State the blood parasite species.
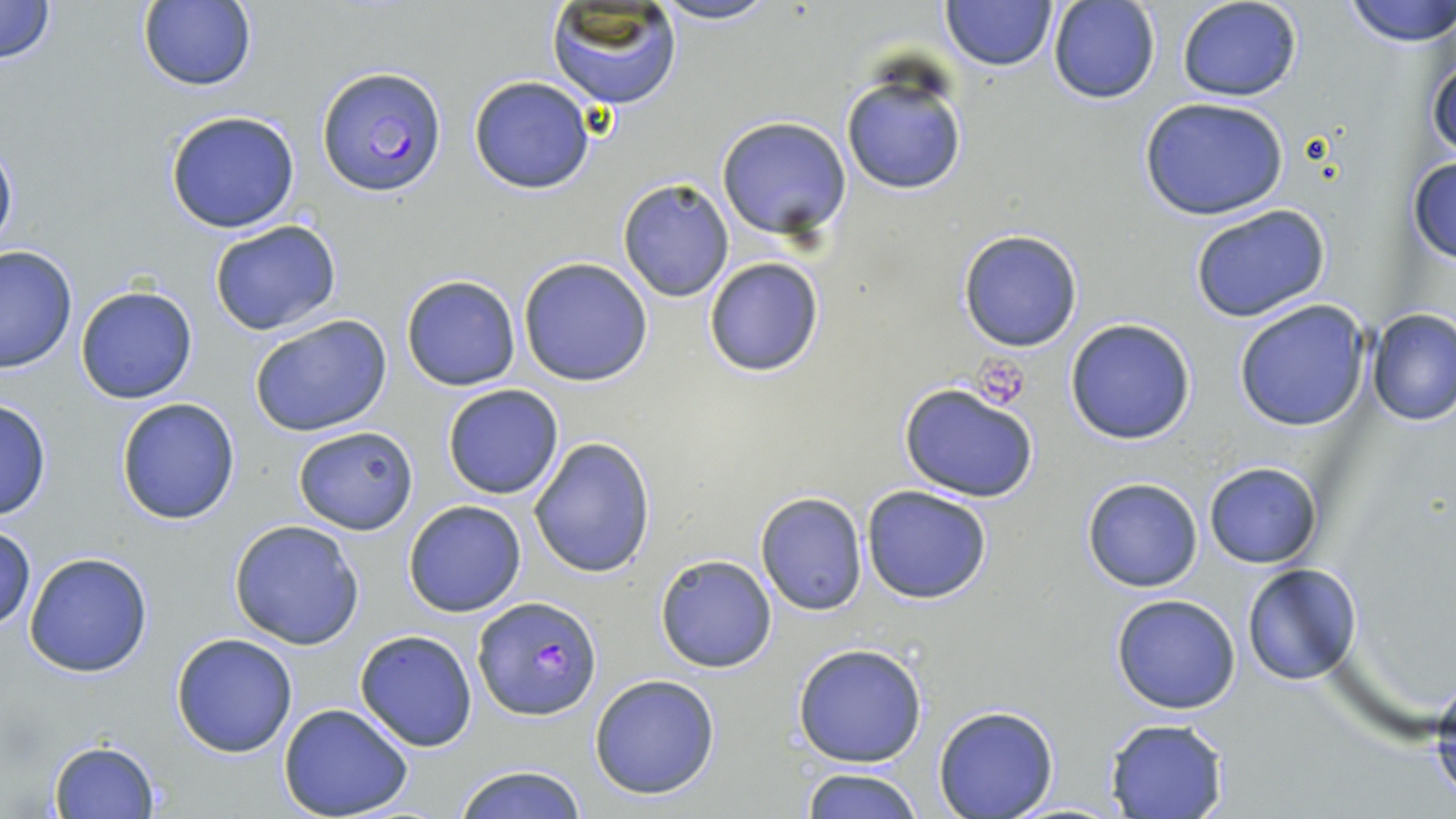

Plasmodium falciparum.

Approximate bounding boxes as (x1, y1, x2, y2) in pixels. Uninfected red blood cell locations: (647, 0, 782, 25), (939, 0, 1057, 71), (1177, 0, 1304, 102), (1341, 0, 1456, 46), (0, 1, 59, 67), (135, 1, 259, 91), (1048, 1, 1160, 105), (544, 2, 683, 109), (1423, 30, 1456, 165), (839, 68, 969, 197), (468, 75, 597, 195), (1139, 96, 1289, 220), (164, 109, 301, 233), (716, 116, 853, 239), (0, 133, 18, 265), (1407, 155, 1455, 266), (617, 177, 736, 303), (1188, 203, 1332, 322), (207, 219, 344, 337), (957, 229, 1083, 352), (1, 246, 76, 373), (703, 256, 825, 378), (518, 257, 653, 387), (400, 275, 521, 391), (75, 284, 199, 405), (1232, 299, 1373, 432), (1367, 310, 1456, 426), (246, 314, 395, 438), (1065, 317, 1197, 444), (897, 383, 1041, 502), (442, 384, 563, 499), (115, 396, 241, 525), (0, 397, 52, 522), (294, 425, 417, 534), (528, 436, 656, 580), (1203, 462, 1322, 569), (1081, 477, 1203, 592), (862, 485, 993, 604), (756, 492, 867, 615), (403, 500, 528, 618), (227, 518, 367, 650), (1, 527, 36, 633), (23, 552, 155, 678), (655, 553, 778, 673), (1242, 565, 1361, 685), (1111, 595, 1240, 714), (355, 630, 477, 751), (170, 633, 299, 757), (792, 642, 928, 768), (1428, 663, 1456, 810), (589, 674, 721, 800), (279, 703, 415, 819), (933, 706, 1058, 819), (1104, 718, 1230, 819), (47, 739, 161, 818), (453, 764, 587, 819), (799, 766, 927, 819). Plasmodium falciparum-infected red blood cell locations: (317, 67, 446, 198), (473, 598, 601, 719). Platelet locations: (975, 356, 1034, 408). Single field of view. Thin blood film. Light microscopy. May-Grünwald-Giemsa-stained preparation. 1000x magnification. Image is 1456×819 pixels.